Identify the parasite.
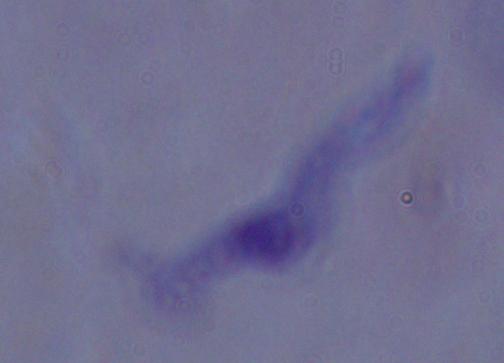

This is a trypanosome.

Summary:
  - Modality: photomicrograph
  - Magnification: 1000x